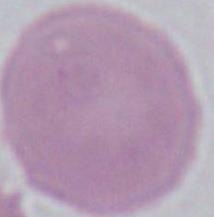
1000x magnification. An erythrocyte is shown. Photomicrograph.